Locate every blood parasite and identify its species.
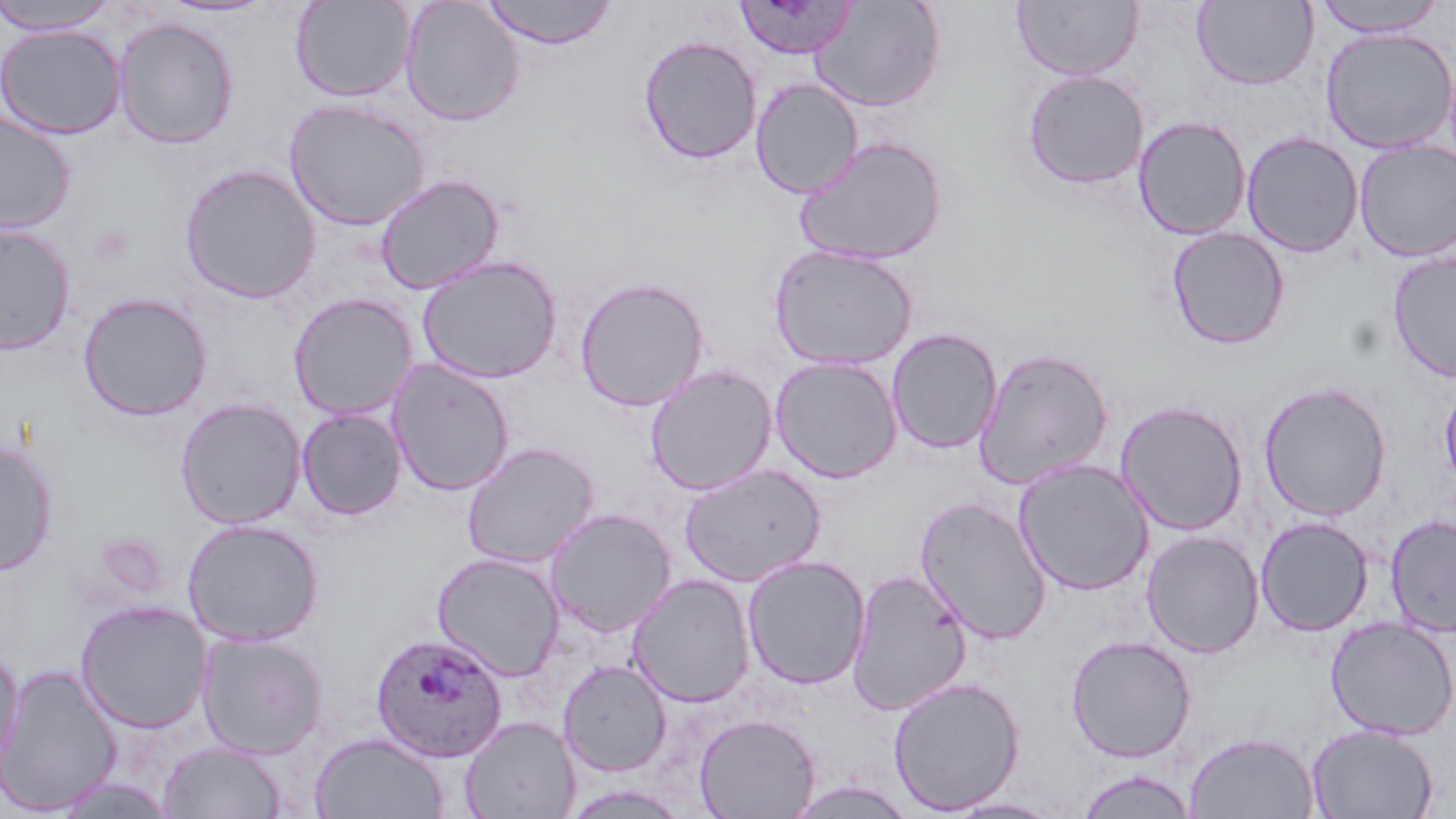

Approximate bounding boxes as (x1,y1)-(x2,y2) corner pairs in pixels.
Plasmodium ovale-infected red blood cells: (370,632)-(509,763).
No Plasmodium falciparum, Plasmodium malariae, Plasmodium vivax, Babesia divergens, or Trypanosoma brucei observed.

Uninfected red blood cell locations: (290,0)-(415,102), (481,0)-(618,49), (1013,0)-(1143,81), (1192,0)-(1319,90), (0,1)-(119,35), (159,1)-(272,17), (399,1)-(523,126), (733,1)-(857,58), (809,1)-(946,112), (1312,1)-(1449,37), (113,16)-(239,149), (0,24)-(126,140), (1320,27)-(1456,154), (638,35)-(761,165), (1022,69)-(1150,189), (750,78)-(863,198), (285,99)-(429,231), (0,110)-(76,234), (1133,116)-(1251,240), (1241,131)-(1364,257), (793,135)-(947,266), (1354,140)-(1456,262), (179,164)-(320,303), (374,174)-(504,294), (0,222)-(76,356), (1166,226)-(1290,350), (769,244)-(919,371), (1387,252)-(1456,383), (416,255)-(562,384), (573,277)-(710,411), (77,293)-(212,421), (288,293)-(418,420), (886,328)-(1002,453), (972,347)-(1114,489), (769,355)-(903,483), (387,359)-(515,497), (644,364)-(777,495), (1439,378)-(1456,497), (1258,382)-(1392,520), (175,398)-(306,528), (1114,399)-(1249,536), (296,408)-(407,521), (0,440)-(59,576), (460,441)-(599,568), (1013,458)-(1155,595), (679,464)-(825,586), (915,496)-(1053,646), (545,508)-(675,636), (1385,514)-(1456,637), (1255,516)-(1374,636), (182,518)-(324,646), (1140,530)-(1264,658), (432,552)-(564,680), (742,555)-(870,690), (847,568)-(973,715), (627,573)-(756,707), (75,600)-(212,733), (1325,617)-(1456,740), (197,632)-(328,759), (1065,635)-(1196,763), (0,643)-(24,772), (558,659)-(672,776), (1,663)-(123,816), (888,676)-(1025,815), (694,713)-(820,819), (460,716)-(579,819), (1307,723)-(1438,819), (1184,731)-(1320,819), (310,732)-(448,819), (159,742)-(286,818), (1075,769)-(1198,819), (51,776)-(176,817), (940,796)-(1067,818). Slide-level diagnosis: Plasmodium ovale. 1000x magnification. Image is 1456×819 pixels. Thin blood film. One field of a larger specimen. May-Grünwald-Giemsa stain. Light microscopy.